Identify the parasite.
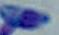
Toxoplasma gondii.

{
  "modality": "photomicrograph",
  "magnification": "1000x"
}